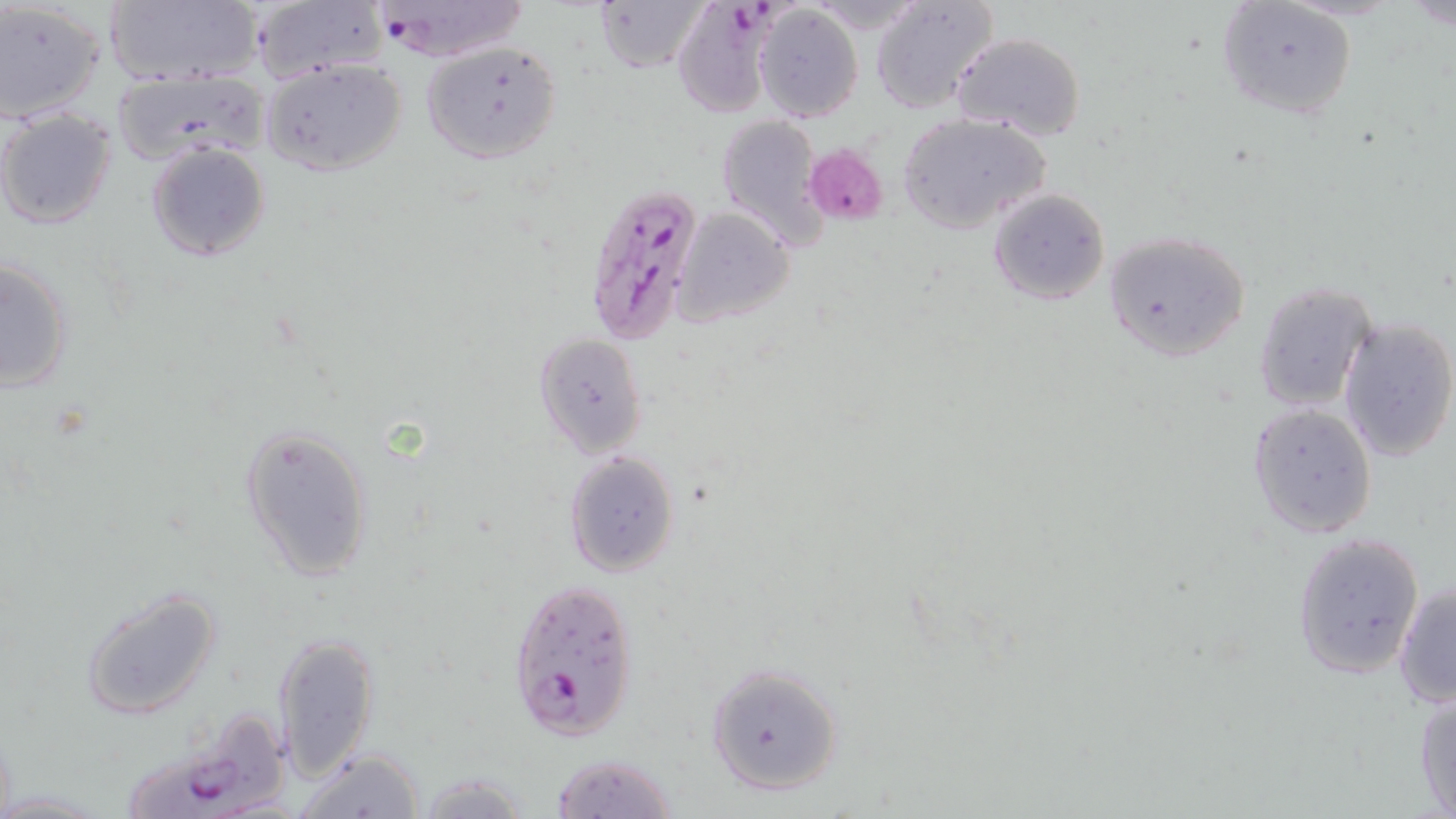

slide-level diagnosis = Plasmodium falciparum
preparation = thin blood film
image size = 1456×819 pixels
modality = optical microscopy
field of view = one of a larger specimen
uninfected red blood cell locations = approximate bounding boxes as named x1/y1/x2/y2 corners in pixels: (x1=104, y1=0, x2=263, y2=88), (x1=594, y1=0, x2=712, y2=72), (x1=872, y1=1, x2=999, y2=114), (x1=0, y1=2, x2=106, y2=126), (x1=1214, y1=2, x2=1356, y2=122), (x1=247, y1=3, x2=384, y2=83), (x1=754, y1=4, x2=864, y2=121), (x1=950, y1=32, x2=1086, y2=141), (x1=421, y1=40, x2=562, y2=165), (x1=261, y1=57, x2=411, y2=177), (x1=110, y1=68, x2=269, y2=166), (x1=0, y1=108, x2=118, y2=230), (x1=896, y1=113, x2=1051, y2=234), (x1=715, y1=114, x2=826, y2=250), (x1=145, y1=142, x2=270, y2=262), (x1=988, y1=187, x2=1110, y2=305), (x1=673, y1=207, x2=795, y2=324), (x1=1103, y1=230, x2=1252, y2=362), (x1=1, y1=258, x2=74, y2=392), (x1=1252, y1=281, x2=1376, y2=412), (x1=1338, y1=316, x2=1456, y2=462), (x1=534, y1=333, x2=649, y2=459), (x1=1249, y1=403, x2=1378, y2=540), (x1=241, y1=422, x2=374, y2=582), (x1=564, y1=450, x2=680, y2=577), (x1=1292, y1=531, x2=1425, y2=677), (x1=1393, y1=581, x2=1455, y2=709), (x1=78, y1=583, x2=225, y2=722), (x1=271, y1=631, x2=379, y2=779), (x1=705, y1=664, x2=844, y2=797), (x1=1413, y1=684, x2=1456, y2=816), (x1=292, y1=746, x2=427, y2=818), (x1=549, y1=752, x2=678, y2=818), (x1=413, y1=774, x2=534, y2=818)
magnification = 1000x
stain = May-Grünwald-Giemsa
Plasmodium falciparum-infected red blood cell locations = approximate bounding boxes as named x1/y1/x2/y2 corners in pixels: (x1=370, y1=1, x2=528, y2=63), (x1=671, y1=4, x2=778, y2=118), (x1=585, y1=182, x2=708, y2=346), (x1=505, y1=576, x2=639, y2=742), (x1=123, y1=706, x2=298, y2=819)
platelet locations = approximate bounding boxes as named x1/y1/x2/y2 corners in pixels: (x1=804, y1=144, x2=889, y2=227)